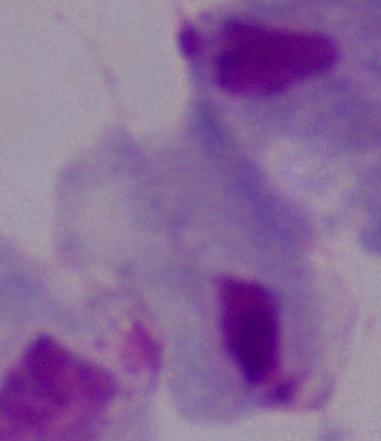
Summary:
  - Magnification: 1000x
  - Modality: micrograph
  - Identification: trichomonad